Classify this cell by malaria status.
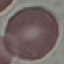

It is uninfected.

Thin smear of blood. Automatically extracted cell patch, resized to 64 × 64 pixels. Giemsa stain. Photographed with a smartphone camera at the microscope eyepiece.